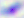

Toxoplasma gondii is shown. 400x magnification. Micrograph.